Report the malaria status of this cell.
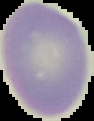
It is uninfected.

image_size: 94×121 pixels
image_type: segmented cell region on a black background
preparation: thin blood film